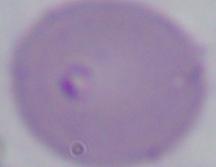
Photomicrograph. 1000x magnification. A Babesia parasite is seen.